State which cell type is depicted.
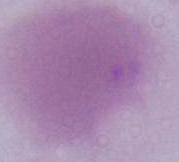
An erythrocyte.

1000x magnification. Photomicrograph.